Report the malaria status of this cell.
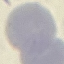
Uninfected.

Summary:
  - Image type: automatically extracted cell patch, resized to 64 × 64 pixels
  - Capture: smartphone through the microscope eyepiece
  - Stain: Giemsa
  - Preparation: thin blood smear